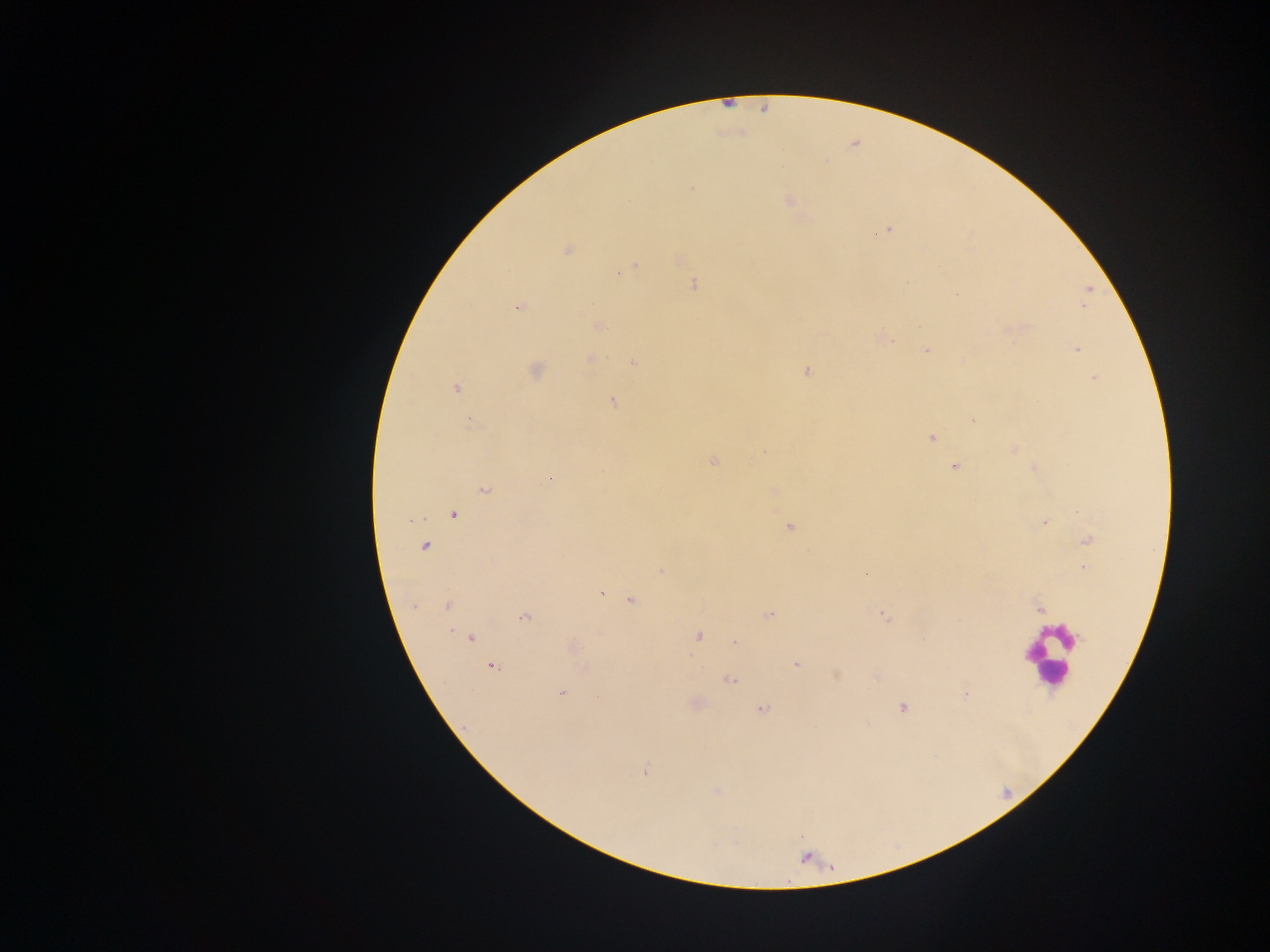
preparation: thick blood smear
field_of_view: single
capture: mobile-phone photograph through a microscope
image_size: 1270×952 pixels
malaria_parasite_locations: 'approximate centers as {x, y} in pixels: {692, 189}, {788, 200}, {888, 230}, {567, 250}, {635, 266}, {907, 283}, {693, 284}, {1089, 289}, {956, 294}, {519, 307}, {1084, 308}, {598, 326}, {889, 340}, {1077, 349}, {926, 350}, {591, 358}, {633, 362}, {535, 370}, {807, 372}, {1093, 378}, {456, 388}, {613, 401}, {973, 420}, {472, 425}, {931, 438}, {1013, 449}, {712, 462}, {954, 466}, {1034, 468}, {549, 478}, {484, 491}, {454, 514}, {410, 520}, {1044, 522}, {790, 527}, {1088, 540}, {425, 546}, {1085, 568}, {660, 571}, {602, 592}, {631, 601}, {414, 606}, {447, 606}, {1040, 609}, {769, 615}, {884, 616}, {523, 617}, {451, 632}, {699, 636}, {471, 638}, {734, 642}, {572, 648}, {796, 665}, {493, 667}, {730, 680}, {561, 693}, {965, 696}, {902, 708}, {761, 709}, {645, 771}, {717, 792}'
country: Ghana
leukocyte_locations: 'approximate centers as {x, y} in pixels: {1049, 656}'